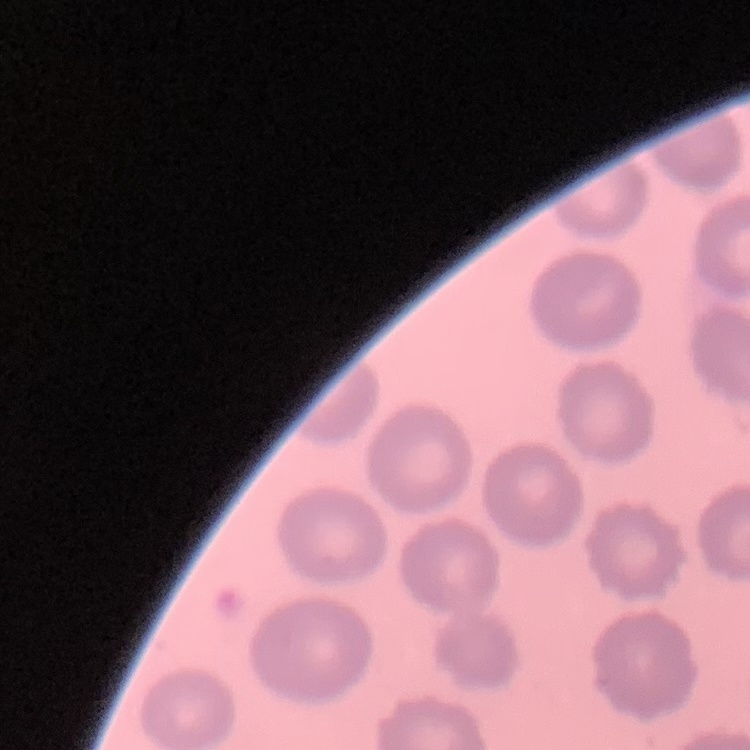 The erythrocytes show no rouleaux formation. Thin peripheral smear. Field's or Giemsa stain. Square crop of a larger photomicrograph.